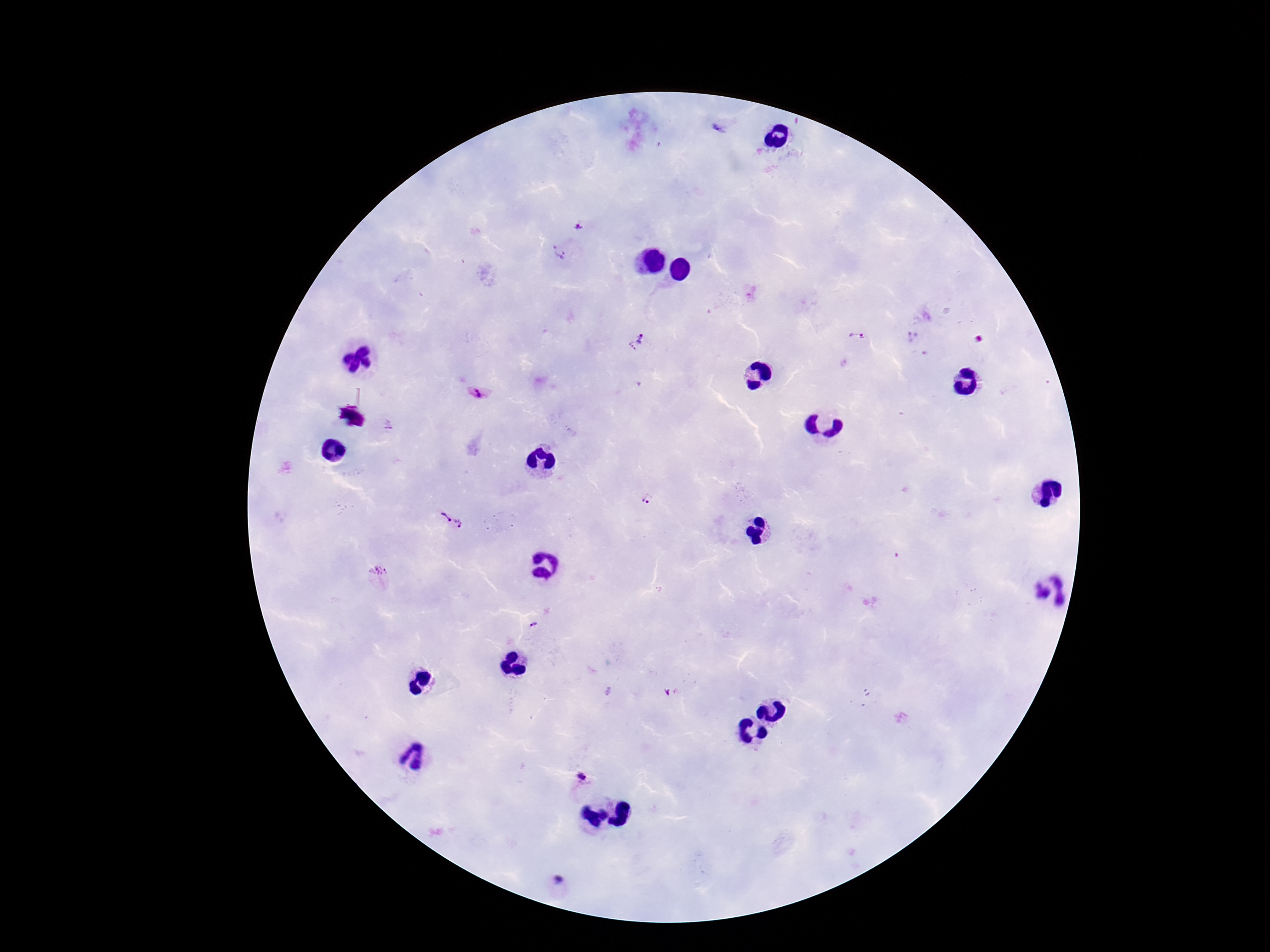

image size = 1270×952 pixels
preparation = thick blood film
stain = Giemsa
patient malaria status = positive
field of view = one from this slide
capture = smartphone camera through the microscope eyepiece
magnification = 100x
Plasmodium parasite locations = approximate object centers, in pixels from the top-left corner: (x=718, y=130), (x=580, y=226), (x=558, y=251), (x=857, y=337), (x=634, y=342), (x=478, y=393), (x=388, y=426), (x=646, y=499), (x=444, y=518), (x=461, y=524), (x=378, y=571), (x=533, y=626), (x=581, y=777), (x=558, y=880)